Report the malaria status of this cell.
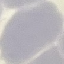
It is uninfected.

stain = Giemsa
image type = cell patch, automatically extracted from a larger field of view and resized to 64 × 64 pixels
preparation = thin blood film
capture = smartphone through the microscope eyepiece